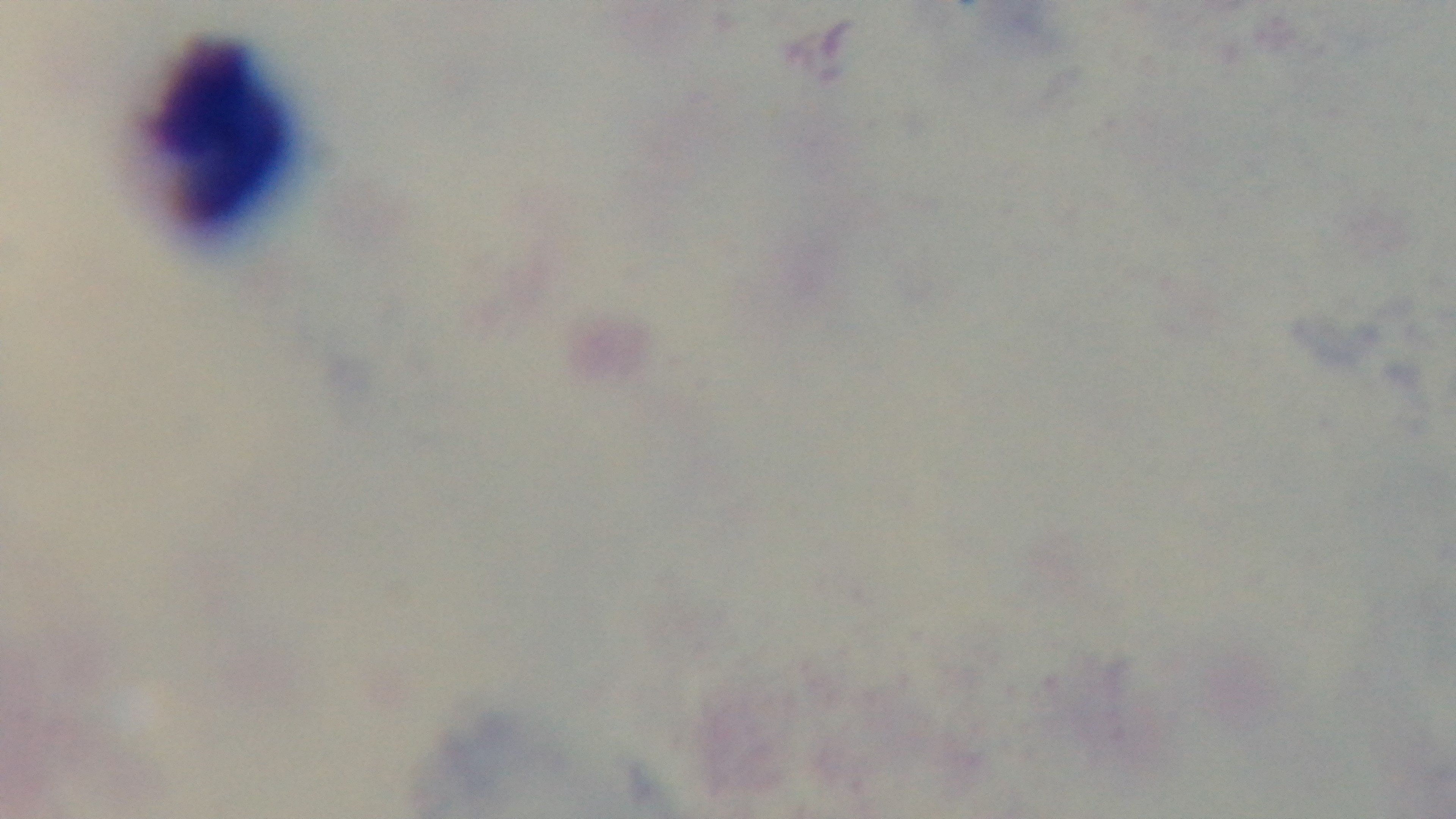

100x oil-immersion objective. Malaria status: uninfected. Captured with a mounted 4K digital camera. Preparation: thick. One field from the slide. Photomicrograph. Giemsa-stained.